Report the malaria status of this cell.
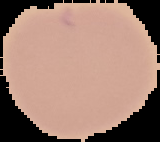
Uninfected.

From a thin blood smear. Segmented cell region on a black background. Image is 160×142 pixels.